Assess the morphology of the erythrocytes.
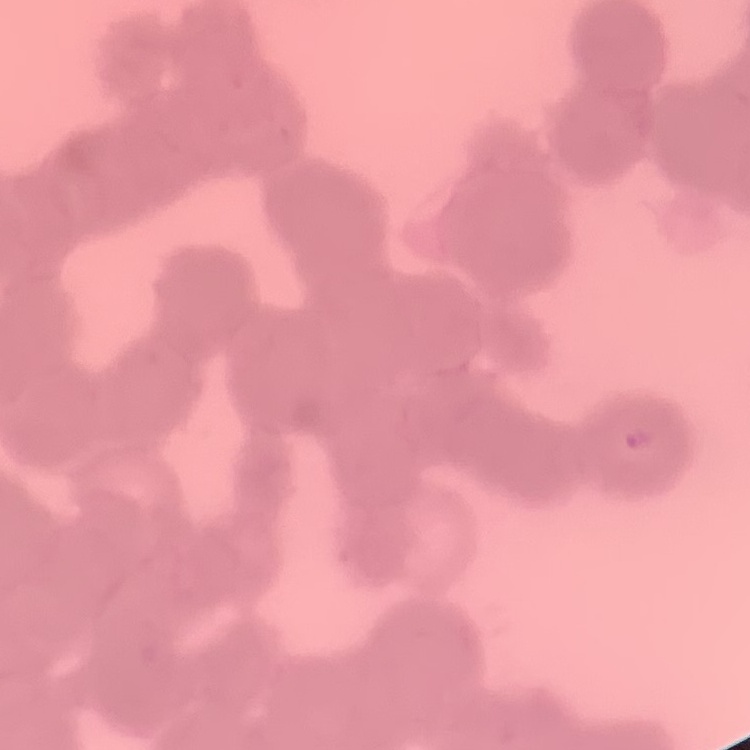
Rouleaux formation.

Field's or Giemsa stain. Thin blood smear. One tile cut from a larger photomicrograph.